Comment on the morphology of the red blood cells.
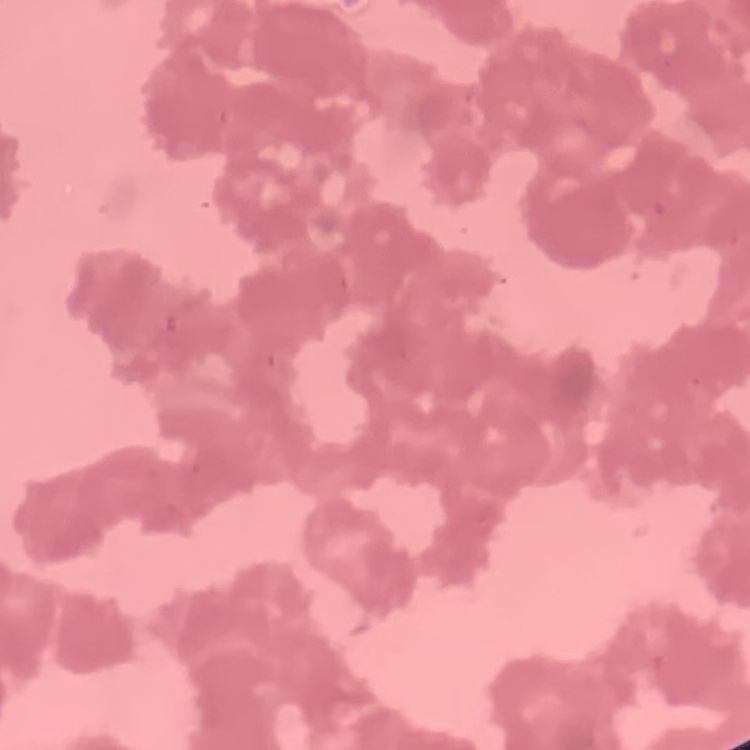

Rouleaux formation.

Summary:
  - Preparation: thin blood film
  - Stain: Field's or Giemsa
  - Image type: one tile cut from a larger photomicrograph